Name the parasite shown.
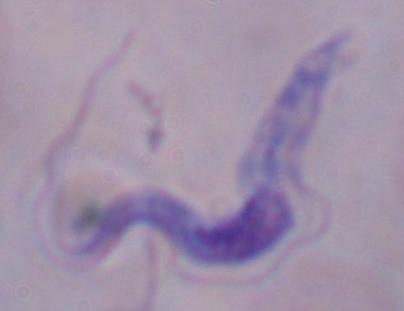
A trypanosome.

magnification = 1000x
modality = micrograph